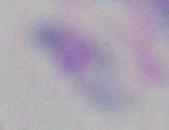

Photomicrograph. Toxoplasma gondii is shown. 1000x magnification.